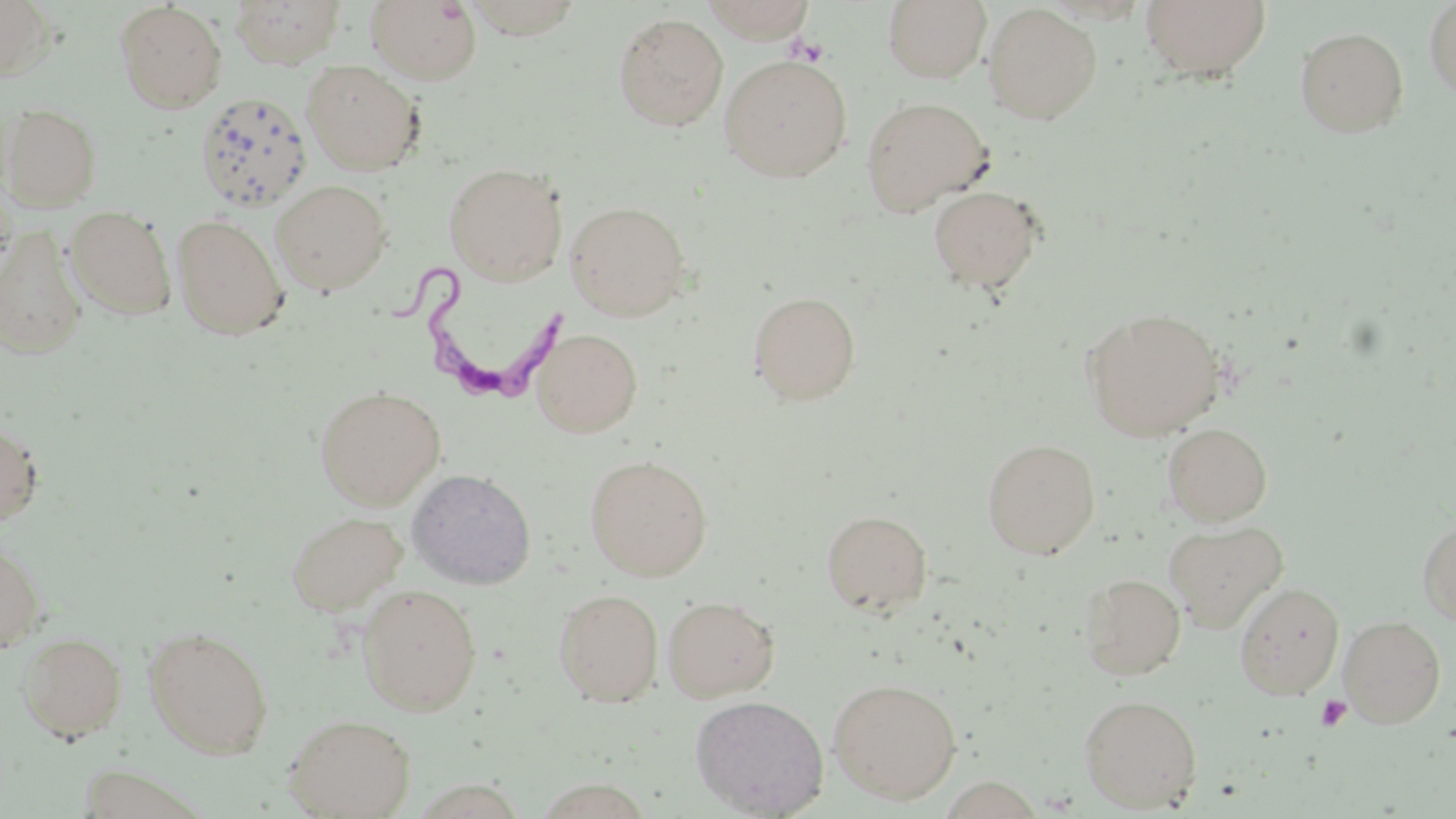

{
  "slide_level_diagnosis": "Trypanosoma brucei",
  "field_of_view": "one of a larger specimen",
  "trypanosoma_brucei_locations": "approximate bounding boxes as [x1, y1, x2, y2] in pixels: [382, 263, 576, 401]",
  "preparation": "thin blood film",
  "modality": "optical microscopy",
  "uninfected_red_blood_cell_locations": "approximate bounding boxes as [x1, y1, x2, y2] in pixels: [0, 0, 57, 83], [700, 0, 818, 42], [1139, 0, 1272, 82], [230, 1, 346, 68], [365, 1, 482, 85], [457, 1, 585, 40], [882, 1, 992, 83], [1423, 1, 1456, 101], [115, 2, 228, 113], [982, 3, 1102, 124], [612, 12, 729, 131], [1295, 26, 1409, 138], [718, 55, 853, 181], [302, 59, 425, 175], [194, 91, 312, 213], [859, 96, 994, 216], [1, 103, 102, 211], [443, 162, 568, 285], [270, 179, 392, 295], [0, 183, 17, 283], [928, 184, 1044, 294], [565, 200, 691, 321], [65, 206, 177, 320], [171, 215, 289, 340], [0, 227, 89, 359], [748, 290, 861, 405], [1082, 307, 1226, 440], [532, 327, 642, 437], [314, 385, 446, 509], [0, 421, 43, 528], [1162, 422, 1273, 525], [982, 438, 1101, 559], [585, 454, 713, 581], [406, 468, 537, 589], [822, 509, 932, 615], [285, 510, 407, 616], [1417, 515, 1456, 627], [1164, 520, 1288, 633], [0, 538, 45, 654], [1079, 573, 1186, 680], [1234, 581, 1344, 698], [357, 583, 483, 716], [553, 588, 664, 706], [662, 594, 780, 702], [1339, 615, 1447, 727], [143, 625, 274, 759], [18, 632, 127, 741], [827, 677, 962, 804], [1078, 693, 1203, 813], [690, 694, 829, 817], [283, 713, 416, 819], [75, 764, 212, 818], [532, 777, 655, 819]",
  "stain": "May-Grünwald-Giemsa",
  "image_size": "1456×819 pixels",
  "magnification": "1000x",
  "platelet_locations": "approximate bounding boxes as [x1, y1, x2, y2] in pixels: [787, 35, 829, 66], [1315, 694, 1352, 731]"
}